Identify the cell.
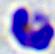

This is a leukocyte.

magnification = 400x
modality = micrograph